Locate and identify every blood parasite.
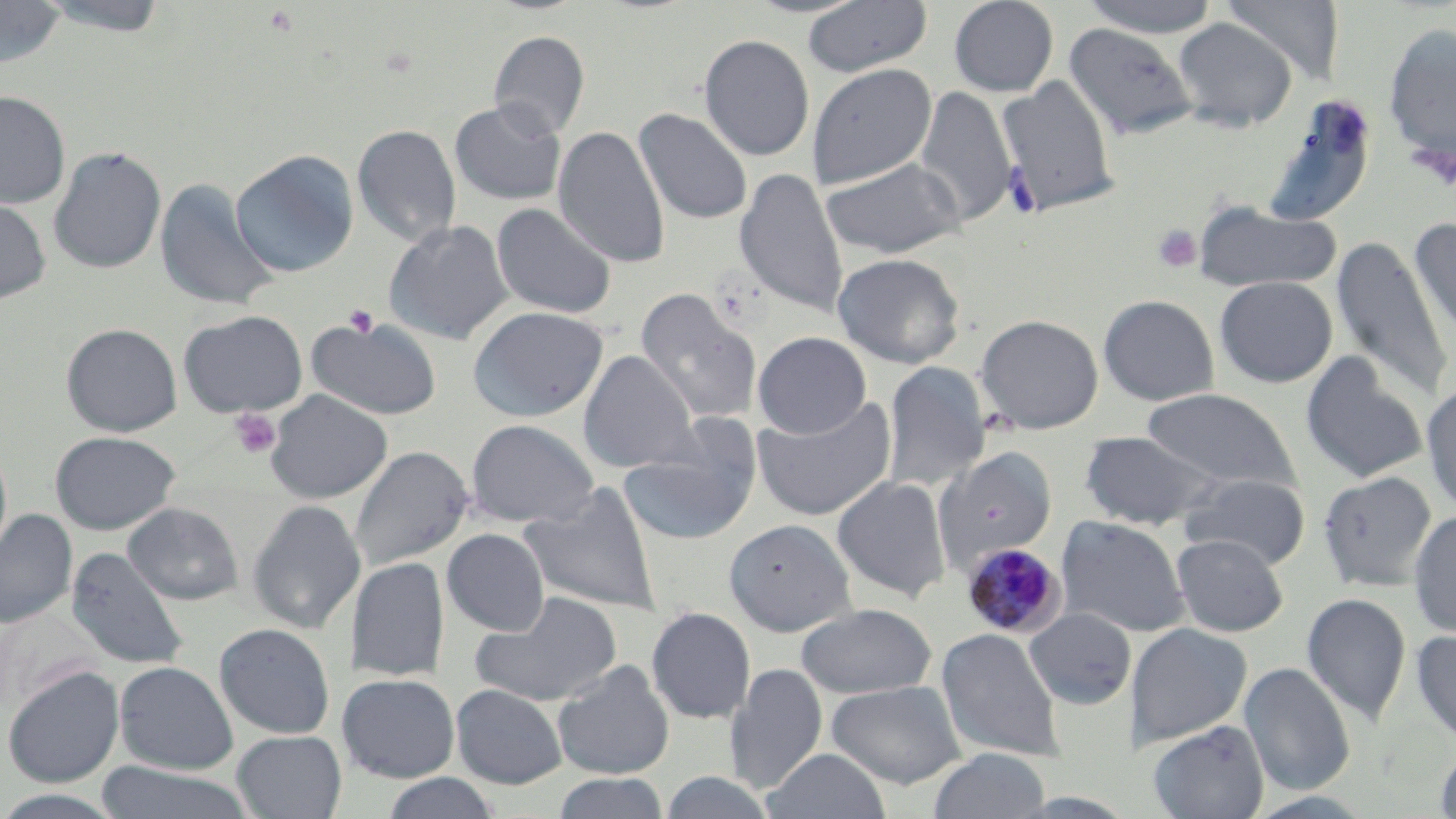
Approximate bounding boxes as named x1/y1/x2/y2 corners in pixels.
Plasmodium malariae-infected red blood cells: (x1=962, y1=543, x2=1066, y2=638).
No Plasmodium falciparum, Plasmodium ovale, Plasmodium vivax, Babesia divergens, or Trypanosoma brucei observed.

Uninfected red blood cell locations: (x1=0, y1=0, x2=66, y2=69), (x1=34, y1=0, x2=173, y2=36), (x1=802, y1=0, x2=932, y2=78), (x1=948, y1=0, x2=1059, y2=97), (x1=1078, y1=0, x2=1222, y2=37), (x1=1221, y1=0, x2=1346, y2=83), (x1=1172, y1=17, x2=1297, y2=132), (x1=1064, y1=22, x2=1199, y2=140), (x1=1383, y1=23, x2=1456, y2=161), (x1=488, y1=30, x2=589, y2=139), (x1=699, y1=34, x2=815, y2=161), (x1=807, y1=62, x2=938, y2=189), (x1=997, y1=74, x2=1120, y2=216), (x1=914, y1=84, x2=1017, y2=228), (x1=0, y1=90, x2=70, y2=209), (x1=1262, y1=97, x2=1377, y2=227), (x1=449, y1=100, x2=566, y2=205), (x1=634, y1=107, x2=754, y2=225), (x1=353, y1=124, x2=461, y2=247), (x1=554, y1=124, x2=670, y2=268), (x1=49, y1=146, x2=166, y2=274), (x1=230, y1=150, x2=359, y2=278), (x1=820, y1=157, x2=964, y2=259), (x1=734, y1=166, x2=849, y2=317), (x1=154, y1=177, x2=279, y2=312), (x1=0, y1=195, x2=52, y2=305), (x1=1192, y1=200, x2=1343, y2=293), (x1=491, y1=203, x2=617, y2=319), (x1=1409, y1=217, x2=1456, y2=348), (x1=384, y1=219, x2=514, y2=344), (x1=1332, y1=235, x2=1453, y2=403), (x1=832, y1=252, x2=965, y2=368), (x1=1214, y1=276, x2=1337, y2=388), (x1=635, y1=290, x2=762, y2=425), (x1=1098, y1=295, x2=1220, y2=406), (x1=468, y1=306, x2=609, y2=422), (x1=178, y1=309, x2=308, y2=418), (x1=975, y1=314, x2=1104, y2=434), (x1=306, y1=316, x2=442, y2=420), (x1=61, y1=322, x2=183, y2=436), (x1=753, y1=332, x2=872, y2=438), (x1=578, y1=350, x2=697, y2=473), (x1=1300, y1=351, x2=1430, y2=483), (x1=599, y1=362, x2=739, y2=520), (x1=882, y1=362, x2=991, y2=491), (x1=1421, y1=381, x2=1456, y2=516), (x1=1141, y1=388, x2=1301, y2=491), (x1=265, y1=391, x2=392, y2=503), (x1=752, y1=395, x2=897, y2=521), (x1=465, y1=419, x2=600, y2=528), (x1=618, y1=423, x2=762, y2=546), (x1=1079, y1=430, x2=1224, y2=530), (x1=50, y1=431, x2=181, y2=534), (x1=0, y1=438, x2=13, y2=567), (x1=349, y1=445, x2=474, y2=572), (x1=936, y1=446, x2=1057, y2=569), (x1=1317, y1=471, x2=1437, y2=591), (x1=1178, y1=472, x2=1311, y2=570), (x1=832, y1=476, x2=951, y2=603), (x1=519, y1=483, x2=662, y2=615), (x1=247, y1=499, x2=366, y2=635), (x1=123, y1=502, x2=243, y2=604), (x1=0, y1=508, x2=77, y2=629), (x1=1408, y1=510, x2=1456, y2=636), (x1=1056, y1=515, x2=1191, y2=638), (x1=724, y1=518, x2=857, y2=636), (x1=442, y1=529, x2=550, y2=636), (x1=1171, y1=534, x2=1288, y2=636), (x1=64, y1=548, x2=189, y2=671), (x1=348, y1=558, x2=449, y2=681), (x1=469, y1=591, x2=623, y2=707), (x1=1301, y1=592, x2=1411, y2=726), (x1=794, y1=603, x2=939, y2=699), (x1=646, y1=607, x2=756, y2=724), (x1=1, y1=608, x2=105, y2=713), (x1=1023, y1=608, x2=1137, y2=709), (x1=214, y1=623, x2=336, y2=739), (x1=1127, y1=623, x2=1253, y2=747), (x1=936, y1=627, x2=1065, y2=763), (x1=1410, y1=628, x2=1456, y2=745), (x1=552, y1=659, x2=676, y2=779), (x1=114, y1=661, x2=238, y2=774), (x1=1239, y1=662, x2=1356, y2=796), (x1=725, y1=664, x2=827, y2=794), (x1=2, y1=666, x2=125, y2=787), (x1=341, y1=673, x2=460, y2=782), (x1=826, y1=679, x2=967, y2=789), (x1=451, y1=683, x2=567, y2=789), (x1=1147, y1=720, x2=1269, y2=819), (x1=232, y1=730, x2=346, y2=818), (x1=1433, y1=743, x2=1456, y2=818), (x1=761, y1=748, x2=891, y2=819), (x1=927, y1=749, x2=1052, y2=819), (x1=93, y1=762, x2=255, y2=819), (x1=656, y1=770, x2=779, y2=818), (x1=552, y1=772, x2=673, y2=818), (x1=378, y1=773, x2=503, y2=819), (x1=0, y1=789, x2=128, y2=818). Platelet locations: (x1=1409, y1=143, x2=1454, y2=189), (x1=1003, y1=164, x2=1042, y2=219), (x1=1152, y1=224, x2=1202, y2=274), (x1=344, y1=305, x2=379, y2=336), (x1=229, y1=408, x2=281, y2=459). Slide-level diagnosis: Plasmodium malariae. Captured at 1000x magnification. Image is 1456×819 pixels. Single field of view. Light microscopy. Thin blood smear. May-Grünwald-Giemsa stain.